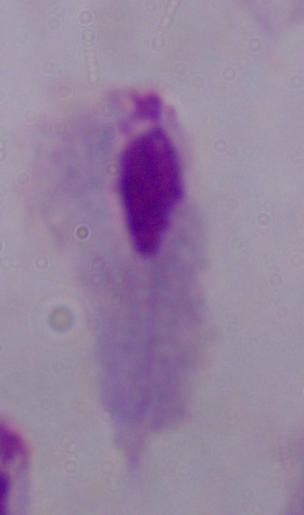 Captured at 1000x magnification. A trichomonad is shown. Photomicrograph.